Report the malaria status of this cell.
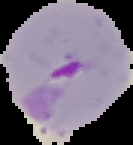
Parasitized.

Summary:
  - Image type: segmented cell region with the area outside set to black
  - Preparation: thin blood film
  - Image size: 133×145 pixels